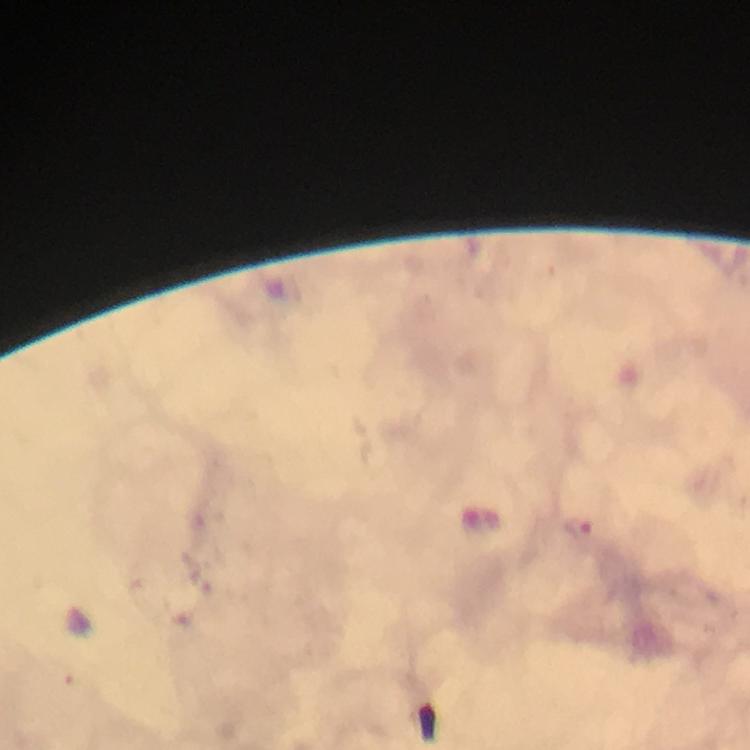
Approximate centers as {x, y} in pixels.
Summary:
  - Malaria parasite locations: {578, 529}
  - Cropped from: a single field of view
  - Image size: 750×750 pixels
  - Magnification: 100x
  - Preparation: thick smear
  - Immersion oil: used
  - Capture: smartphone camera through the microscope
  - Stain: Giemsa
  - Context: from a malaria diagnostic workup